Give the preparation type.
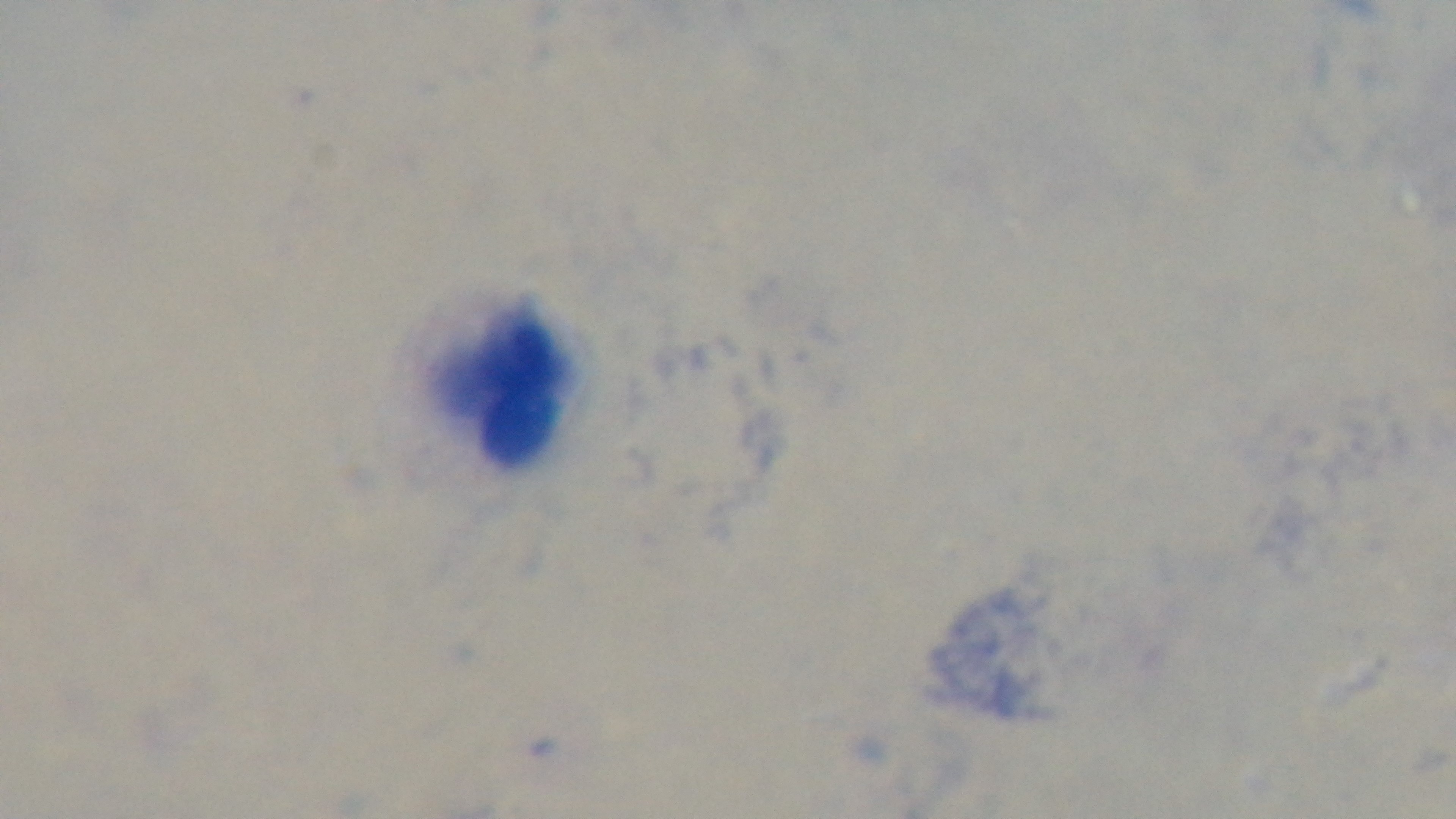
Thick.

modality: light microscopy
malaria_status: negative
field_of_view: single
objective: 100x oil immersion
capture: mounted 4K digital camera
stain: Giemsa